Identify the parasite.
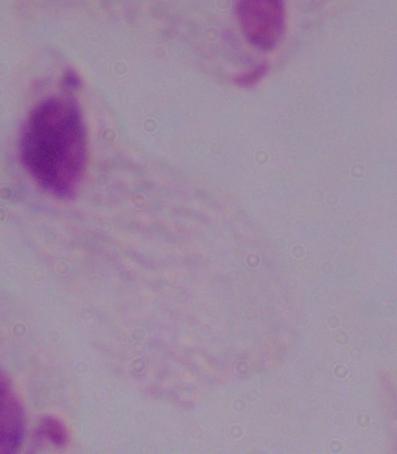

A trichomonad.

modality = micrograph
magnification = 1000x